State the blood parasite species.
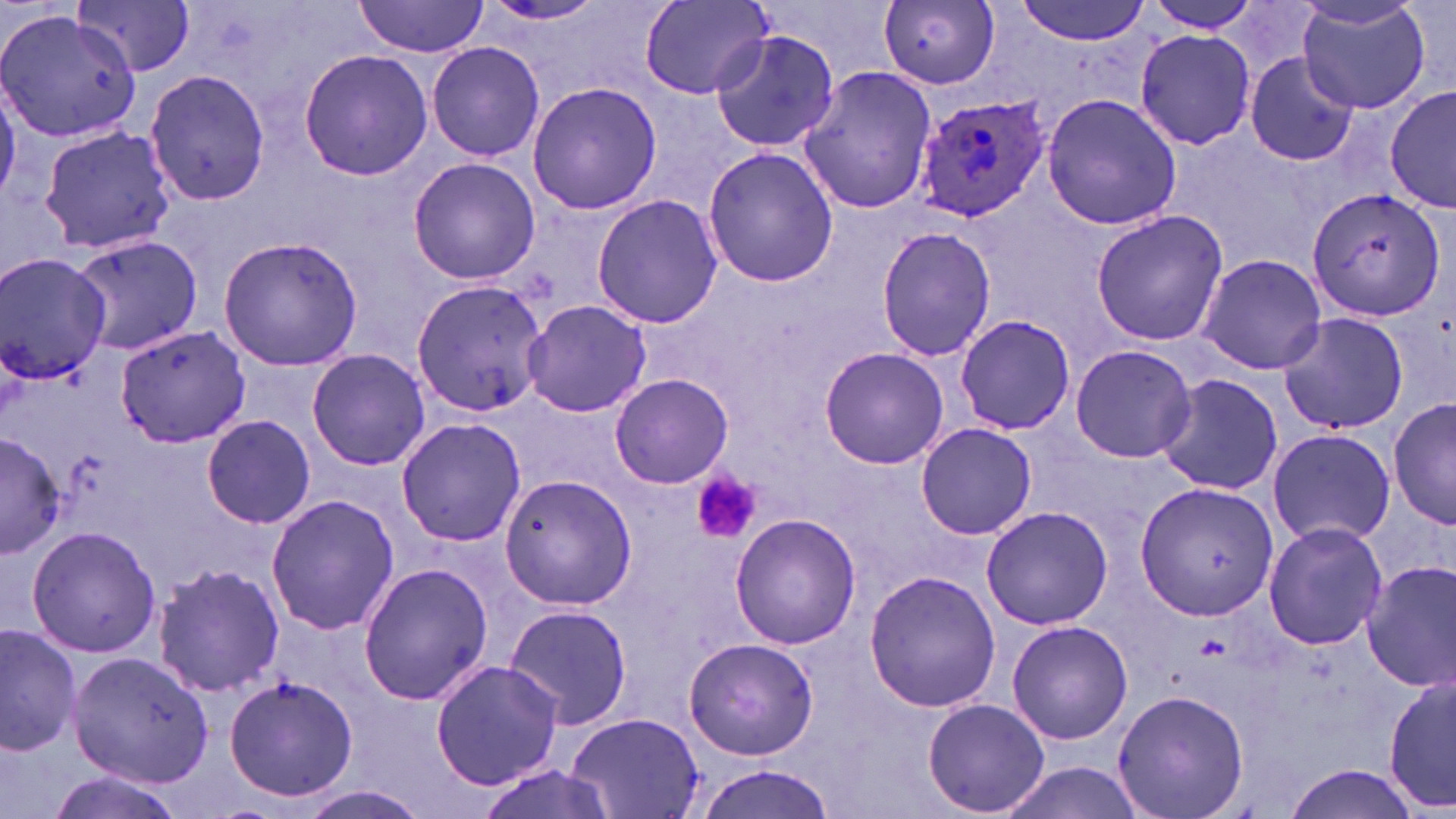

Plasmodium ovale.

modality = optical microscopy
uninfected red blood cell locations = approximate bounding boxes as (x1,y1)-(x2,y2) corner pairs in pixels: (355,0)-(487,57), (1014,0)-(1149,44), (1142,0)-(1265,32), (1295,0)-(1431,113), (75,1)-(196,77), (477,1)-(614,26), (641,1)-(774,99), (879,1)-(1000,88), (0,9)-(139,142), (1135,27)-(1256,151), (709,28)-(841,155), (426,42)-(546,162), (299,50)-(433,180), (1243,53)-(1359,167), (798,64)-(939,215), (144,65)-(273,208), (0,75)-(21,206), (527,82)-(663,214), (1386,86)-(1455,213), (1042,92)-(1183,232), (38,124)-(176,254), (702,146)-(841,288), (408,157)-(541,284), (1305,185)-(1446,322), (591,195)-(725,329), (1090,208)-(1227,346), (875,226)-(997,361), (68,233)-(202,355), (217,236)-(365,372), (1197,252)-(1327,375), (2,253)-(113,387), (411,280)-(549,417), (523,299)-(652,419), (1276,311)-(1410,436), (954,313)-(1077,435), (112,324)-(251,448), (1070,345)-(1197,463), (818,347)-(950,468), (305,349)-(432,470), (1155,373)-(1284,497), (611,374)-(733,489), (1389,397)-(1454,532), (201,416)-(317,529), (395,417)-(527,547), (915,423)-(1035,538), (1267,427)-(1395,547), (0,431)-(63,561), (498,473)-(638,611), (1135,482)-(1279,621), (266,494)-(401,635), (980,505)-(1113,630), (729,513)-(862,648), (1262,521)-(1389,650), (27,526)-(159,658), (1360,559)-(1456,690), (357,562)-(492,707), (151,563)-(284,697), (864,570)-(1000,712), (504,603)-(632,729), (1006,620)-(1133,745), (0,624)-(80,755), (682,636)-(819,760), (68,651)-(217,790), (431,659)-(564,789), (1383,671)-(1456,818), (224,672)-(359,805), (1112,689)-(1249,819), (922,699)-(1050,817), (567,710)-(706,817), (997,760)-(1148,819), (1283,763)-(1424,819), (697,765)-(836,819), (47,770)-(188,819), (291,786)-(430,819)
magnification = 1000x
Plasmodium ovale-infected red blood cell locations = approximate bounding boxes as (x1,y1)-(x2,y2) corner pairs in pixels: (914,96)-(1054,223)
platelet locations = approximate bounding boxes as (x1,y1)-(x2,y2) corner pairs in pixels: (689,472)-(761,546)
image size = 1456×819 pixels
field of view = one of a larger specimen
preparation = thin blood film
stain = May-Grünwald-Giemsa